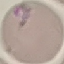

malaria status = parasitized
image type = automatically extracted cell patch, resized to 64 × 64 pixels
stain = Giemsa
preparation = thin smear
capture = smartphone camera at the microscope eyepiece